Assess this cell for malaria.
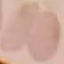
It is uninfected.

Summary:
  - Capture: smartphone camera at the microscope eyepiece
  - Stain: Giemsa
  - Image type: automatically extracted cell patch, resized to 64 × 64 pixels
  - Preparation: thin smear